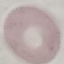

Malaria status: uninfected. Thin blood smear. Acquired by smartphone through the microscope eyepiece. Automatically extracted cell patch, resized to 64 × 64 pixels. Giemsa-stained preparation.